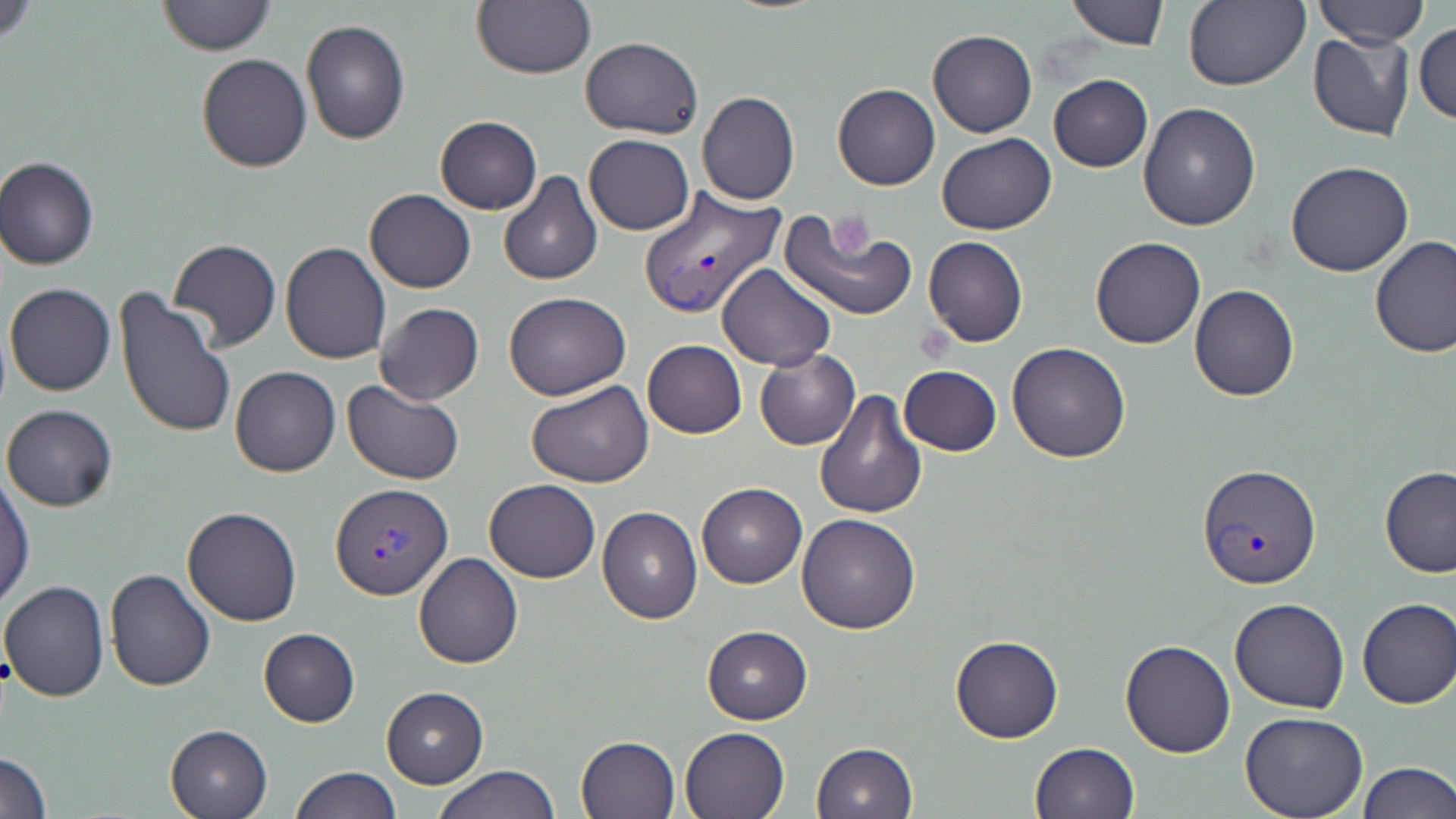

Approximate bounding boxes as named x1/y1/x2/y2 corners in pixels. Platelet locations: (x1=831, y1=211, x2=879, y2=254). Plasmodium vivax-infected red blood cell locations: (x1=638, y1=187, x2=786, y2=321), (x1=1199, y1=464, x2=1320, y2=589), (x1=330, y1=483, x2=453, y2=600). Uninfected red blood cell locations: (x1=0, y1=0, x2=46, y2=44), (x1=158, y1=0, x2=276, y2=54), (x1=472, y1=0, x2=595, y2=80), (x1=1311, y1=0, x2=1428, y2=48), (x1=1066, y1=1, x2=1169, y2=49), (x1=1185, y1=1, x2=1310, y2=91), (x1=300, y1=19, x2=412, y2=146), (x1=1415, y1=21, x2=1456, y2=124), (x1=928, y1=31, x2=1037, y2=137), (x1=1307, y1=31, x2=1415, y2=143), (x1=580, y1=35, x2=702, y2=138), (x1=196, y1=53, x2=310, y2=173), (x1=1047, y1=74, x2=1152, y2=172), (x1=832, y1=83, x2=939, y2=190), (x1=698, y1=92, x2=801, y2=205), (x1=1137, y1=102, x2=1260, y2=230), (x1=435, y1=116, x2=542, y2=214), (x1=937, y1=132, x2=1055, y2=235), (x1=584, y1=135, x2=694, y2=235), (x1=1, y1=156, x2=100, y2=270), (x1=1286, y1=162, x2=1415, y2=277), (x1=498, y1=171, x2=602, y2=287), (x1=364, y1=189, x2=476, y2=294), (x1=778, y1=208, x2=916, y2=322), (x1=923, y1=236, x2=1028, y2=348), (x1=1090, y1=237, x2=1205, y2=349), (x1=1369, y1=237, x2=1456, y2=358), (x1=167, y1=239, x2=282, y2=352), (x1=280, y1=243, x2=392, y2=365), (x1=716, y1=263, x2=834, y2=370), (x1=5, y1=283, x2=116, y2=398), (x1=1190, y1=285, x2=1299, y2=402), (x1=114, y1=288, x2=237, y2=441), (x1=504, y1=292, x2=632, y2=400), (x1=374, y1=302, x2=485, y2=406), (x1=644, y1=339, x2=746, y2=438), (x1=1006, y1=343, x2=1130, y2=463), (x1=754, y1=350, x2=858, y2=450), (x1=899, y1=364, x2=1002, y2=456), (x1=230, y1=366, x2=341, y2=477), (x1=343, y1=380, x2=465, y2=486), (x1=528, y1=380, x2=654, y2=489), (x1=812, y1=388, x2=926, y2=519), (x1=2, y1=404, x2=118, y2=512), (x1=1379, y1=467, x2=1456, y2=578), (x1=0, y1=474, x2=34, y2=609), (x1=484, y1=479, x2=600, y2=583), (x1=696, y1=482, x2=805, y2=588), (x1=597, y1=505, x2=703, y2=624), (x1=181, y1=506, x2=303, y2=626), (x1=797, y1=512, x2=921, y2=635), (x1=413, y1=553, x2=523, y2=669), (x1=104, y1=569, x2=217, y2=692), (x1=1, y1=580, x2=111, y2=702), (x1=1356, y1=597, x2=1455, y2=709), (x1=1231, y1=598, x2=1349, y2=714), (x1=702, y1=625, x2=812, y2=724), (x1=258, y1=627, x2=360, y2=727), (x1=949, y1=635, x2=1064, y2=744), (x1=1119, y1=637, x2=1235, y2=757), (x1=381, y1=687, x2=488, y2=787), (x1=1238, y1=711, x2=1368, y2=819), (x1=165, y1=724, x2=273, y2=818), (x1=679, y1=725, x2=790, y2=819), (x1=575, y1=735, x2=680, y2=819), (x1=812, y1=742, x2=918, y2=818), (x1=1029, y1=742, x2=1141, y2=819), (x1=0, y1=750, x2=52, y2=818), (x1=1355, y1=761, x2=1455, y2=817), (x1=432, y1=764, x2=561, y2=819), (x1=290, y1=766, x2=400, y2=819). Slide-level diagnosis: Plasmodium vivax. Light microscopy. Image is 1456×819 pixels. Single field of view. Captured at 1000x magnification. Thin blood smear. May-Grünwald-Giemsa stain.